Outline each blood parasite and name the species.
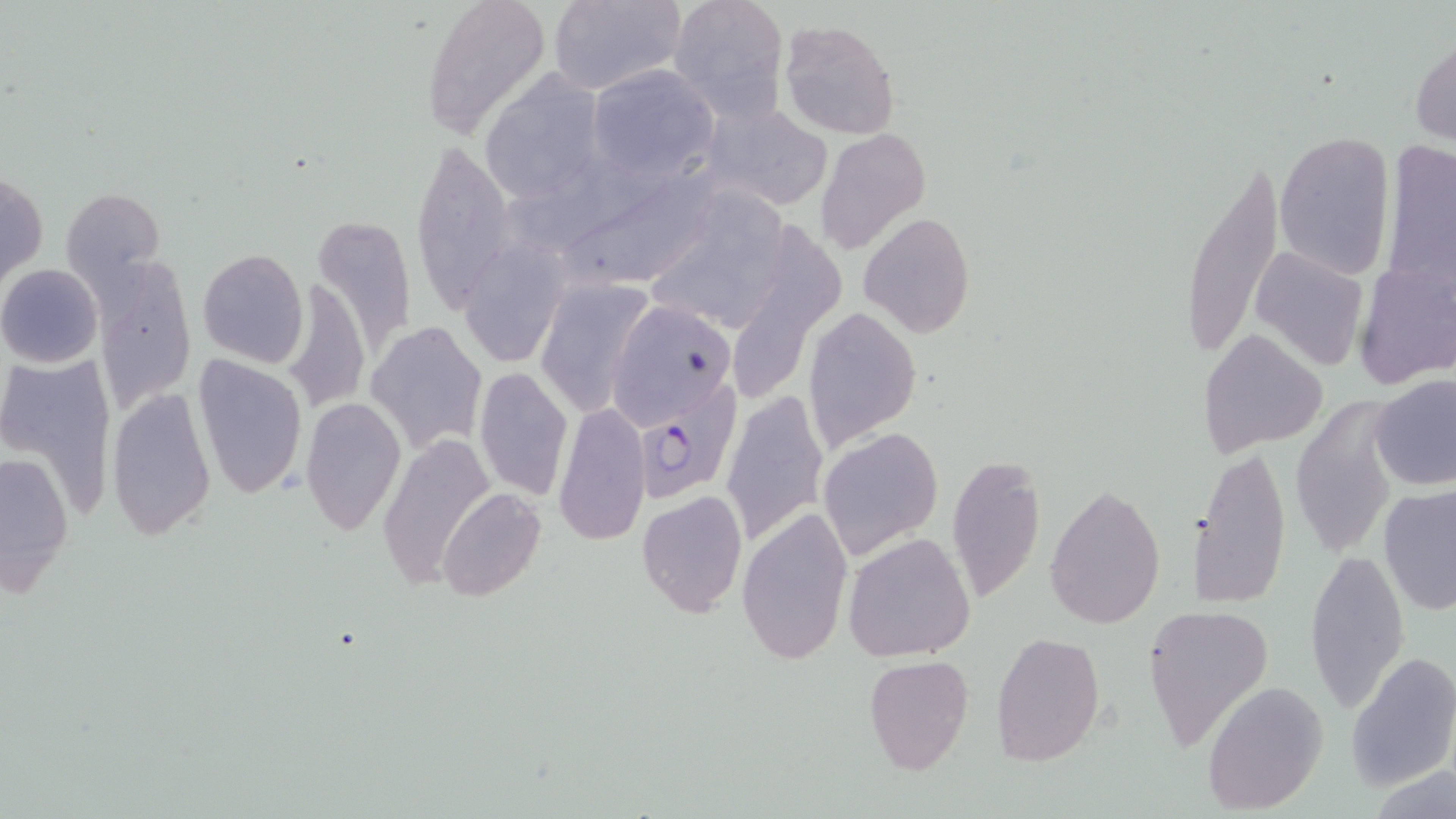

Approximate bounding boxes as named x1/y1/x2/y2 corners in pixels.
Plasmodium falciparum-infected red blood cells: (x1=630, y1=370, x2=752, y2=511).
No Plasmodium ovale, Plasmodium malariae, Plasmodium vivax, Babesia divergens, or Trypanosoma brucei observed.

Summary:
  - Uninfected red blood cell locations: (x1=422, y1=0, x2=552, y2=138), (x1=546, y1=0, x2=684, y2=96), (x1=667, y1=0, x2=790, y2=117), (x1=779, y1=18, x2=899, y2=140), (x1=1411, y1=38, x2=1456, y2=148), (x1=587, y1=66, x2=717, y2=181), (x1=477, y1=73, x2=607, y2=208), (x1=706, y1=104, x2=830, y2=210), (x1=816, y1=127, x2=931, y2=255), (x1=1275, y1=132, x2=1396, y2=277), (x1=410, y1=138, x2=517, y2=314), (x1=1176, y1=155, x2=1288, y2=370), (x1=576, y1=162, x2=728, y2=294), (x1=1, y1=168, x2=46, y2=295), (x1=62, y1=188, x2=164, y2=291), (x1=643, y1=189, x2=794, y2=338), (x1=312, y1=211, x2=417, y2=356), (x1=859, y1=213, x2=975, y2=337), (x1=456, y1=238, x2=573, y2=371), (x1=1248, y1=244, x2=1370, y2=374), (x1=196, y1=249, x2=308, y2=368), (x1=1355, y1=254, x2=1455, y2=391), (x1=90, y1=255, x2=196, y2=411), (x1=0, y1=264, x2=103, y2=368), (x1=532, y1=277, x2=654, y2=415), (x1=602, y1=298, x2=737, y2=429), (x1=802, y1=306, x2=922, y2=452), (x1=365, y1=322, x2=486, y2=452), (x1=1197, y1=328, x2=1330, y2=456), (x1=191, y1=353, x2=307, y2=501), (x1=3, y1=354, x2=116, y2=519), (x1=473, y1=365, x2=573, y2=502), (x1=1370, y1=374, x2=1456, y2=491), (x1=105, y1=387, x2=217, y2=541), (x1=719, y1=390, x2=830, y2=549), (x1=300, y1=398, x2=405, y2=536), (x1=553, y1=400, x2=651, y2=547), (x1=1288, y1=402, x2=1397, y2=560), (x1=816, y1=427, x2=943, y2=557), (x1=378, y1=433, x2=493, y2=590), (x1=0, y1=444, x2=74, y2=603), (x1=1187, y1=447, x2=1292, y2=610), (x1=945, y1=455, x2=1046, y2=602), (x1=1044, y1=483, x2=1165, y2=628), (x1=1377, y1=486, x2=1454, y2=615), (x1=437, y1=487, x2=547, y2=602), (x1=636, y1=490, x2=748, y2=618), (x1=738, y1=506, x2=852, y2=665), (x1=843, y1=532, x2=977, y2=663), (x1=1306, y1=547, x2=1410, y2=712), (x1=1143, y1=603, x2=1274, y2=746), (x1=992, y1=630, x2=1105, y2=766), (x1=1347, y1=652, x2=1456, y2=792), (x1=864, y1=655, x2=973, y2=775), (x1=1199, y1=682, x2=1328, y2=813)
  - Slide-level diagnosis: Plasmodium falciparum
  - Modality: optical microscopy
  - Field of view: one of a larger specimen
  - Image size: 1456×819 pixels
  - Magnification: 1000x
  - Preparation: thin blood film
  - Stain: May-Grünwald-Giemsa